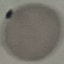

result = no malaria parasites seen
stain = Giemsa
image type = cell patch, automatically extracted from a larger field of view and resized to 64 × 64 pixels
capture = smartphone through the microscope eyepiece
preparation = thin smear